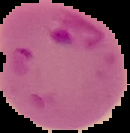
{
  "preparation": "thin blood film",
  "malaria_status": "parasitized",
  "image_size": "130×133 pixels",
  "image_type": "segmented cell region on a black background"
}